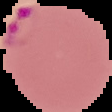
From a thin blood smear. The area outside the segmented cell region is set to black. Image is 112×112 pixels. Result: malaria parasites identified.